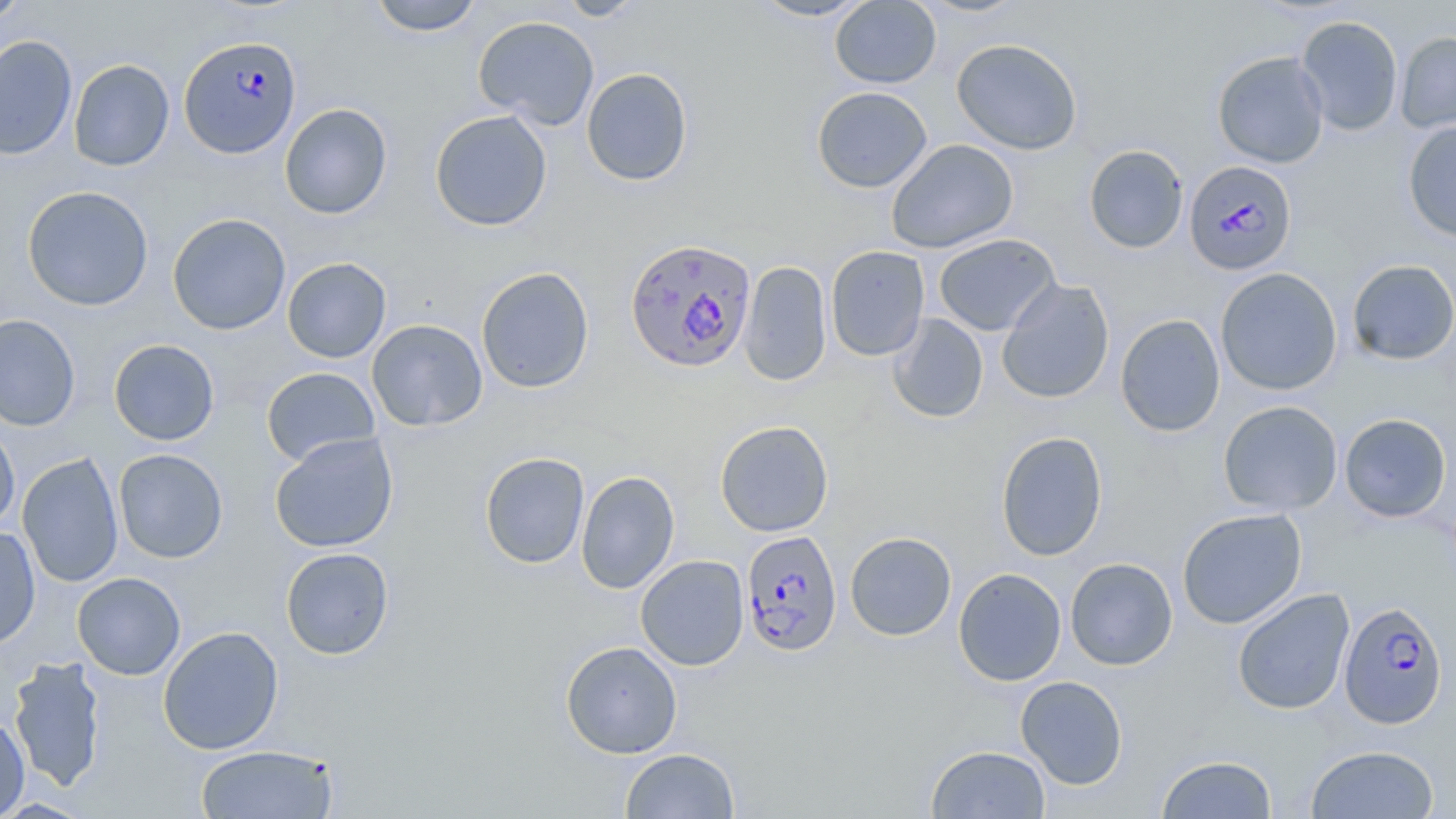

Summary:
  - Coordinate format: approximate bounding boxes as (x1,y1)-(x2,y2) corner pairs in pixels
  - Uninfected red blood cell locations: (0,0)-(30,25), (368,0)-(484,36), (557,0)-(646,21), (749,0)-(874,21), (830,0)-(941,89), (916,0)-(1029,17), (1295,15)-(1404,136), (473,16)-(600,129), (1394,31)-(1456,134), (0,35)-(77,160), (952,38)-(1082,155), (1212,50)-(1329,168), (68,59)-(174,171), (581,67)-(694,186), (812,87)-(932,193), (279,103)-(393,219), (429,110)-(553,232), (1402,121)-(1456,243), (886,139)-(1018,254), (1083,145)-(1189,253), (22,185)-(154,311), (167,213)-(291,335), (933,234)-(1061,336), (825,245)-(930,361), (282,257)-(392,363), (1346,259)-(1456,366), (738,260)-(832,386), (476,267)-(595,393), (1215,267)-(1343,396), (996,278)-(1115,404), (886,313)-(988,423), (0,314)-(81,431), (1115,314)-(1225,437), (366,319)-(488,431), (108,338)-(220,445), (261,366)-(381,467), (1217,400)-(1343,516), (1339,413)-(1452,522), (0,420)-(20,534), (714,420)-(833,537), (996,431)-(1108,561), (269,432)-(399,553), (113,449)-(228,563), (479,451)-(590,569), (17,452)-(124,588), (576,470)-(680,594), (1177,507)-(1307,629), (0,527)-(41,649), (845,531)-(957,641), (280,547)-(394,660), (635,555)-(749,671), (1065,557)-(1178,670), (953,568)-(1067,686), (72,572)-(186,680), (1231,588)-(1355,715), (158,626)-(285,755), (561,640)-(682,758), (8,657)-(106,792), (1016,676)-(1128,789), (0,714)-(30,818), (195,744)-(340,818), (925,744)-(1051,819), (1305,745)-(1439,818), (620,748)-(739,819), (1157,754)-(1278,818)
  - Plasmodium falciparum-infected red blood cell locations: (178,35)-(301,159), (1184,159)-(1300,276), (625,236)-(758,372), (741,529)-(843,657), (1339,601)-(1448,729)
  - Slide-level diagnosis: Plasmodium falciparum
  - Stain: May-Grünwald-Giemsa
  - Field of view: single
  - Magnification: 1000x
  - Modality: optical microscopy
  - Image size: 1456×819 pixels
  - Preparation: thin blood smear